Comment on the morphology of the erythrocytes.
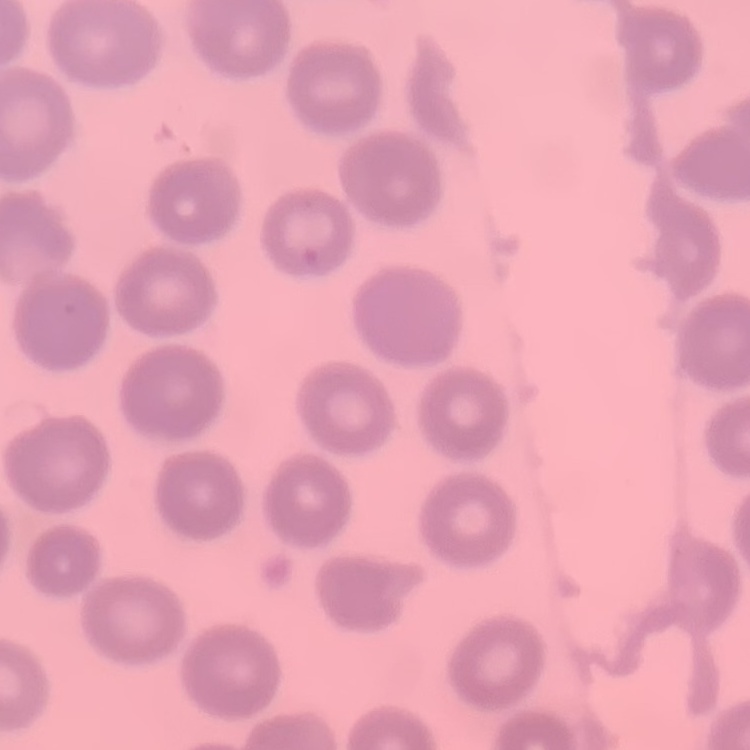

They show no rouleaux formation.

Summary:
  - Preparation: thin peripheral smear
  - Stain: Field's or Giemsa
  - Image type: square crop of a larger photomicrograph